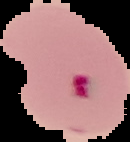
Summary:
  - Image type: segmented cell region with the area outside set to black
  - Malaria status: parasitized
  - Image size: 130×142 pixels
  - Preparation: thin blood film